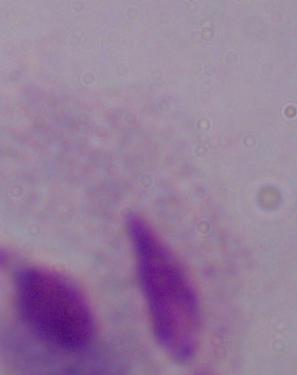
Summary:
  - Modality: micrograph
  - Magnification: 1000x
  - Identification: trichomonad